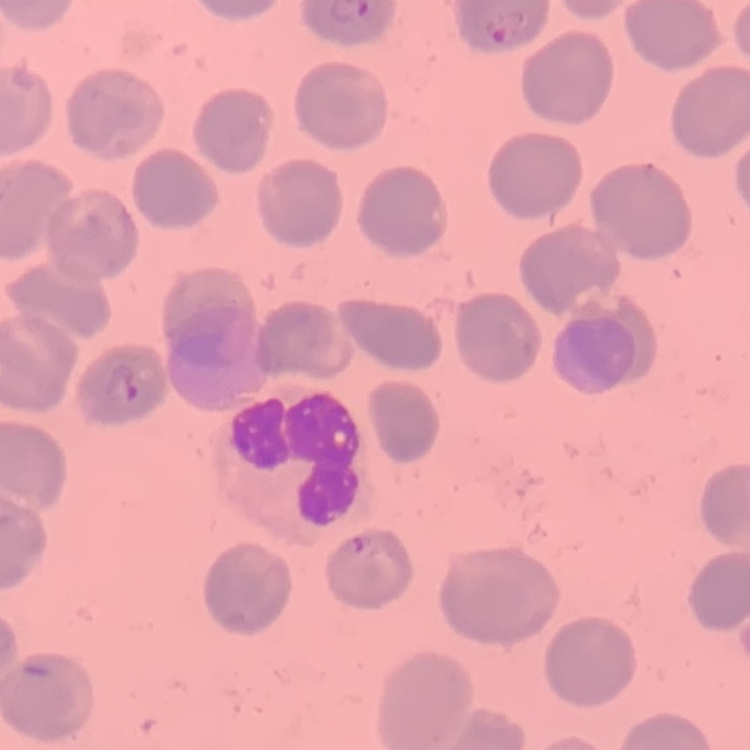

Summary:
  - Red blood cell morphology: no rouleaux formation
  - Stain: Field's or Giemsa
  - Preparation: thin peripheral smear
  - Image type: square crop of a larger photomicrograph